Identify the parasite.
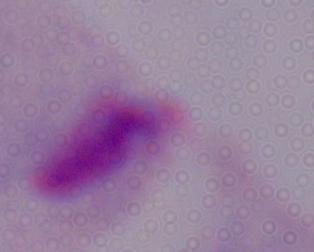

A trichomonad.

Summary:
  - Magnification: 1000x
  - Modality: photomicrograph